Give the extent of all uninfected red blood cells.
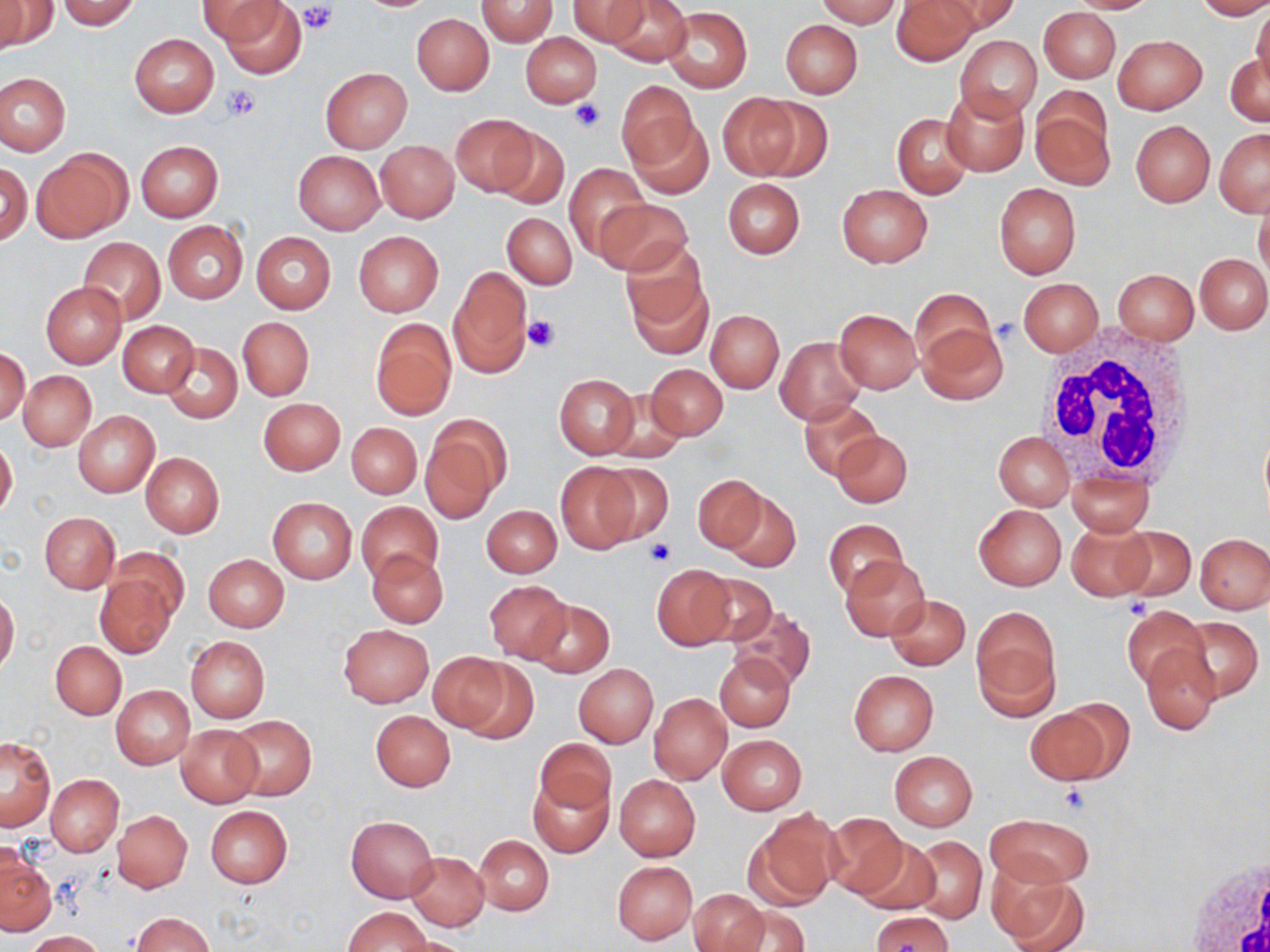
Approximate bounding boxes as (x1, y1, x2, y2) in pixels.
Uninfected red blood cells: (56, 0, 143, 29), (198, 0, 287, 46), (476, 0, 558, 46), (566, 0, 650, 46), (603, 0, 692, 67), (815, 0, 904, 27), (892, 0, 979, 66), (935, 0, 1021, 34), (1066, 0, 1161, 14), (1193, 0, 1270, 20), (1, 1, 55, 51), (215, 1, 307, 78), (662, 7, 751, 93), (1039, 7, 1120, 82), (1251, 7, 1270, 93), (412, 13, 494, 95), (780, 19, 862, 98), (520, 32, 601, 107), (130, 33, 220, 117), (955, 35, 1042, 121), (1114, 35, 1207, 114), (1225, 53, 1269, 127), (321, 67, 412, 152), (0, 73, 70, 155), (614, 81, 701, 174), (941, 86, 1028, 175), (718, 93, 805, 180), (1030, 93, 1114, 190), (751, 97, 834, 182), (892, 112, 974, 199), (450, 114, 538, 196), (627, 117, 715, 199), (1131, 121, 1215, 206), (493, 128, 569, 209), (1214, 128, 1270, 216), (135, 140, 223, 222), (376, 141, 458, 222), (33, 148, 130, 243), (293, 150, 384, 236), (0, 162, 31, 244), (565, 163, 647, 261), (723, 178, 805, 258), (993, 181, 1081, 279), (837, 185, 932, 267), (1254, 197, 1270, 284), (595, 199, 691, 277), (502, 213, 577, 288), (162, 220, 249, 304), (353, 231, 443, 316), (251, 232, 336, 314), (78, 237, 166, 325), (621, 245, 711, 351), (1195, 253, 1270, 333), (448, 265, 532, 376), (1112, 269, 1198, 344), (1019, 279, 1103, 355), (41, 281, 126, 368), (910, 289, 998, 370), (833, 309, 922, 392), (706, 310, 783, 392), (237, 317, 314, 401), (371, 319, 456, 420), (118, 321, 199, 396), (917, 322, 1010, 404), (775, 336, 866, 424), (162, 343, 242, 422), (1, 348, 29, 425), (645, 363, 727, 440), (19, 371, 96, 451), (554, 374, 640, 457), (600, 391, 691, 465), (258, 397, 345, 475), (799, 399, 885, 481), (73, 410, 159, 497), (421, 421, 506, 522), (347, 423, 421, 499), (831, 431, 913, 509), (993, 431, 1074, 509), (0, 438, 18, 519), (141, 452, 224, 537), (554, 462, 641, 555), (592, 464, 675, 544), (1066, 468, 1156, 536), (693, 475, 768, 552), (722, 491, 800, 573), (268, 497, 357, 584), (357, 501, 442, 584), (973, 503, 1066, 590), (482, 505, 561, 577), (39, 512, 120, 594), (823, 519, 907, 599), (1066, 522, 1154, 600), (1113, 526, 1196, 601), (1196, 534, 1270, 613), (107, 545, 189, 627), (368, 550, 448, 628), (203, 554, 288, 632), (840, 555, 930, 641), (652, 564, 737, 649), (693, 572, 778, 647), (94, 575, 175, 658), (483, 580, 571, 663), (0, 590, 20, 675), (884, 595, 970, 670), (529, 598, 613, 676), (727, 605, 817, 691), (1120, 605, 1209, 690), (971, 609, 1060, 718), (1175, 616, 1262, 704), (339, 625, 432, 707), (186, 636, 270, 722), (51, 640, 126, 720), (1140, 646, 1220, 733), (427, 652, 517, 735), (714, 652, 795, 732), (573, 663, 658, 748), (848, 670, 938, 756), (111, 685, 194, 769), (648, 692, 732, 784), (1025, 706, 1115, 785), (370, 711, 455, 791), (228, 714, 317, 800), (177, 724, 263, 807), (719, 735, 806, 814), (0, 738, 56, 831), (534, 738, 614, 817), (889, 751, 977, 830), (528, 773, 614, 858), (45, 774, 123, 856), (614, 774, 700, 861), (205, 806, 292, 888), (112, 809, 193, 893), (744, 809, 842, 911), (985, 812, 1096, 888), (822, 813, 907, 901), (346, 816, 438, 902), (473, 835, 553, 916), (850, 836, 942, 915), (905, 836, 987, 924), (1, 850, 55, 937), (406, 851, 489, 930), (613, 861, 697, 944), (989, 871, 1088, 952), (689, 890, 767, 952), (725, 905, 811, 952), (343, 906, 432, 951), (868, 910, 954, 950), (131, 913, 214, 951), (25, 930, 107, 951), (391, 935, 474, 952).

Summary:
  - White blood cell locations: (1034, 330, 1200, 486), (1178, 848, 1270, 952)
  - Platelet locations: (299, 2, 336, 35), (219, 84, 259, 123), (569, 99, 607, 132), (523, 312, 559, 352), (647, 537, 676, 566), (1125, 597, 1152, 619), (1059, 784, 1093, 814)
  - Slide-level diagnosis: no evidence of blood parasites
  - Stain: May-Grünwald-Giemsa
  - Magnification: 1000x
  - Preparation: thin blood smear
  - Field of view: one of a larger specimen
  - Image size: 1270×952 pixels
  - Modality: optical microscopy